Classify this cell by malaria status.
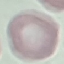

Uninfected.

capture = smartphone camera at the microscope eyepiece
stain = Giemsa
image type = automatically extracted cell patch, resized to 64 × 64 pixels
preparation = thin blood smear